Describe the morphology of the erythrocytes.
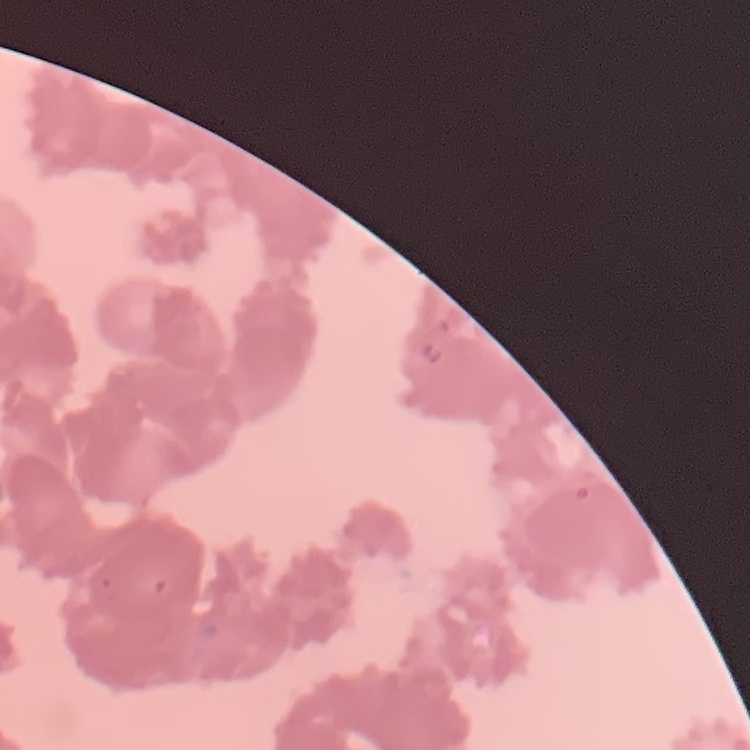
They show rouleaux formation.

{
  "stain": "Field's or Giemsa",
  "image_type": "square crop of a larger photomicrograph",
  "preparation": "thin peripheral smear"
}